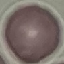

Summary:
  - Result: no malaria parasites seen
  - Preparation: thin blood smear
  - Image type: cell patch, automatically extracted from a larger field of view and resized to 64 × 64 pixels
  - Stain: Giemsa
  - Capture: smartphone through the microscope eyepiece